State the preparation type.
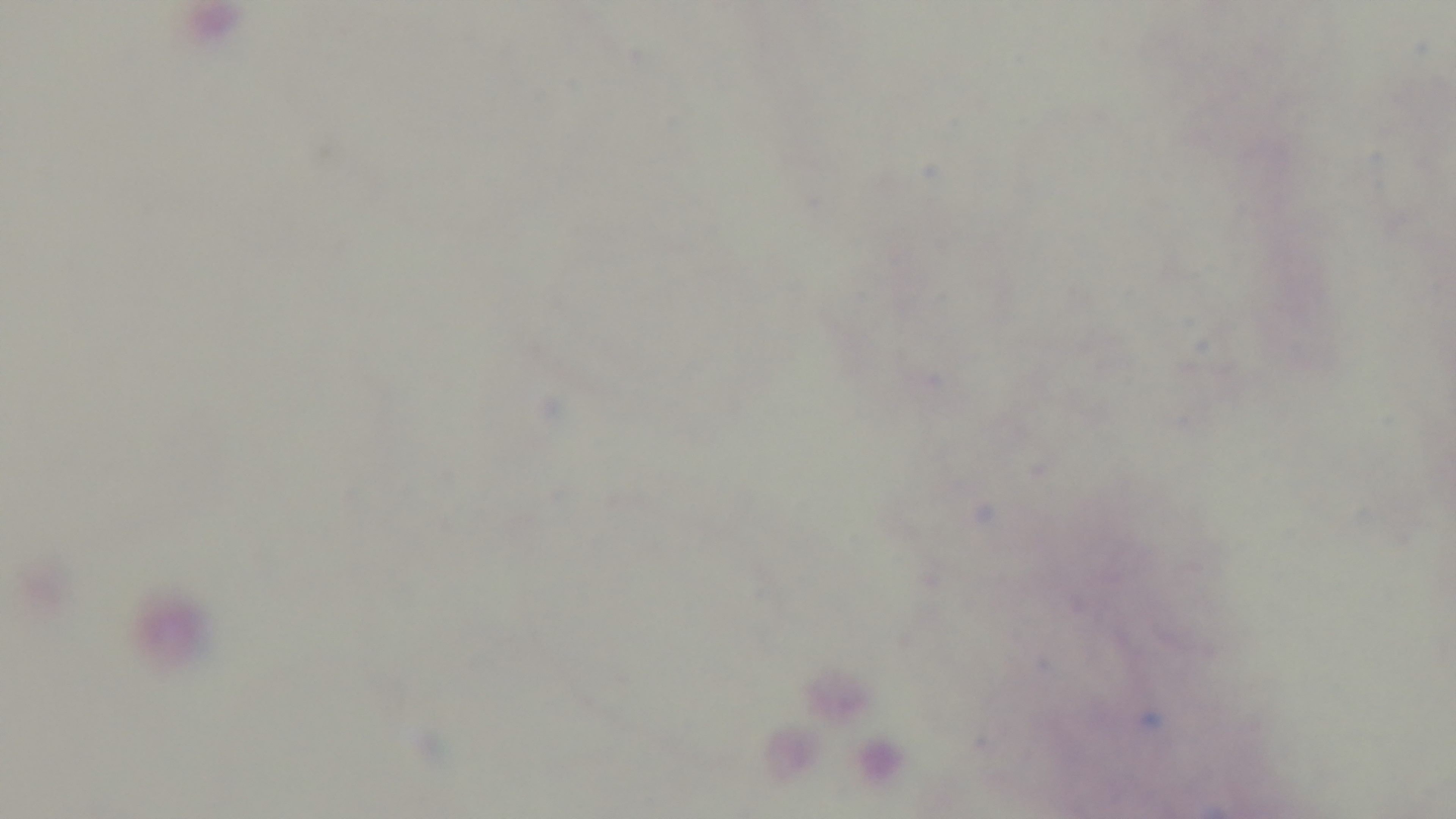

It is a thick blood film.

capture: mounted 4K digital camera
malaria_status: negative
objective: 100x oil immersion
modality: light microscopy
field_of_view: single
stain: Giemsa